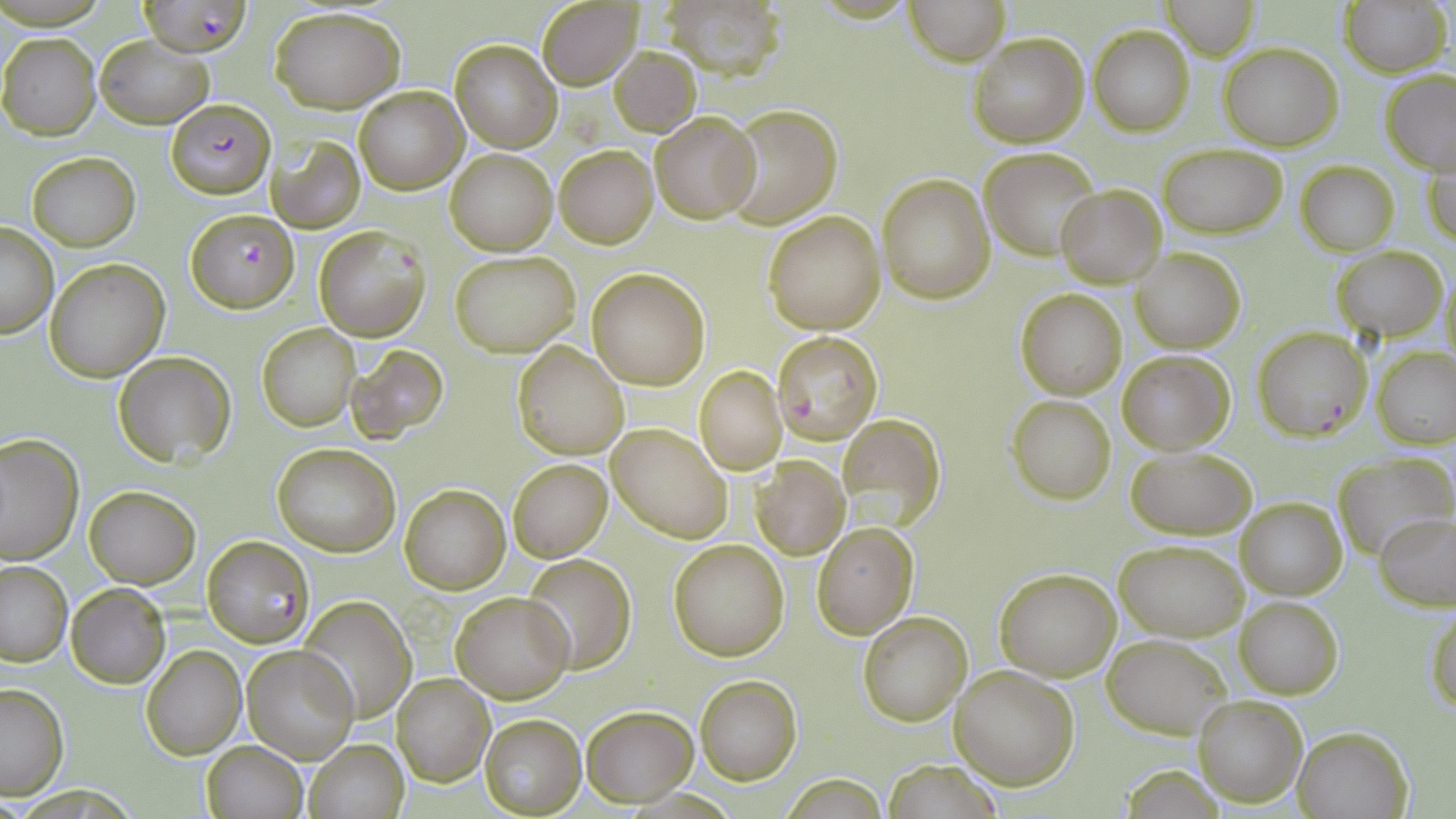

Summary:
  - Coordinate format: approximate bounding boxes as (x1, y1, x2, y2) in pixels
  - Plasmodium falciparum-infected red blood cell locations: (143, 0, 249, 58), (166, 98, 274, 198), (189, 210, 297, 312), (314, 226, 429, 342), (1253, 326, 1372, 442), (770, 330, 882, 443), (201, 535, 314, 647)
  - Uninfected red blood cell locations: (536, 0, 644, 90), (658, 0, 789, 83), (902, 0, 1010, 66), (1337, 0, 1451, 76), (1160, 1, 1259, 59), (270, 6, 406, 112), (1089, 25, 1194, 135), (968, 31, 1088, 149), (0, 33, 101, 140), (95, 36, 213, 127), (449, 38, 563, 153), (1219, 42, 1342, 150), (608, 45, 701, 136), (1379, 70, 1455, 174), (353, 85, 467, 194), (722, 104, 844, 228), (649, 111, 759, 222), (267, 136, 366, 233), (1425, 142, 1456, 247), (1157, 144, 1288, 237), (554, 145, 657, 248), (980, 145, 1102, 260), (446, 149, 556, 254), (27, 152, 140, 251), (1296, 161, 1398, 256), (878, 173, 993, 303), (1057, 184, 1167, 287), (763, 210, 885, 333), (0, 221, 59, 337), (1332, 246, 1446, 343), (1132, 249, 1245, 353), (449, 250, 581, 357), (44, 259, 170, 382), (1440, 262, 1455, 371), (586, 269, 710, 390), (1015, 287, 1128, 399), (258, 323, 360, 431), (513, 341, 629, 460), (348, 345, 449, 443), (1372, 347, 1456, 449), (1117, 350, 1233, 453), (112, 351, 236, 466), (694, 365, 787, 474), (1007, 394, 1116, 504), (839, 414, 946, 526), (607, 422, 731, 542), (0, 433, 83, 565), (272, 442, 400, 555), (1125, 446, 1255, 539), (1332, 452, 1454, 559), (749, 456, 850, 559), (508, 458, 612, 561), (401, 484, 510, 593), (84, 486, 200, 588), (1236, 497, 1346, 600), (1375, 512, 1456, 611), (813, 522, 918, 638), (668, 538, 790, 660), (1114, 539, 1248, 641), (521, 555, 637, 676), (0, 561, 72, 666), (995, 568, 1120, 680), (65, 581, 170, 688), (450, 591, 574, 705), (1236, 596, 1343, 699), (298, 597, 416, 722), (1428, 607, 1456, 713), (858, 611, 972, 727), (1104, 635, 1231, 739), (140, 646, 246, 761), (242, 646, 357, 763), (949, 665, 1079, 790), (391, 674, 495, 786), (696, 676, 803, 785), (0, 684, 69, 799), (1192, 693, 1307, 808), (582, 706, 696, 806), (480, 714, 587, 817), (1292, 724, 1414, 818), (304, 740, 409, 818), (201, 741, 309, 819), (880, 760, 1005, 818), (779, 772, 888, 816)
  - Slide-level diagnosis: Plasmodium falciparum
  - Stain: May-Grünwald-Giemsa
  - Image size: 1456×819 pixels
  - Field of view: one of a larger specimen
  - Preparation: thin blood smear
  - Modality: optical microscopy
  - Magnification: 1000x